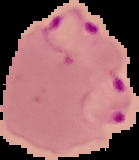

Summary:
  - Image size: 139×160 pixels
  - Preparation: thin blood smear
  - Image type: segmented cell region on a black background
  - Result: malaria parasites detected